Assess the morphology of the erythrocytes.
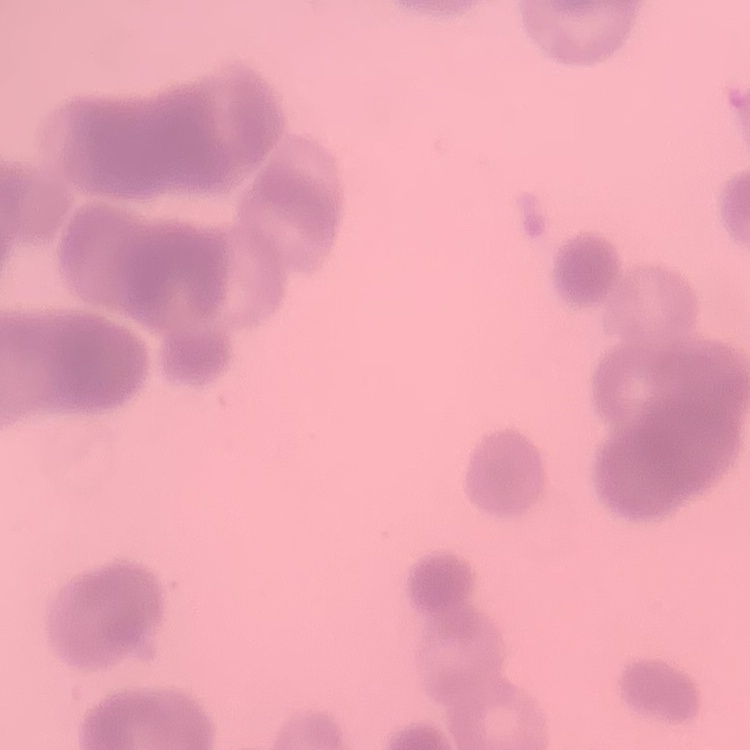
Rouleaux formation.

Summary:
  - Preparation: thin blood film
  - Stain: Field's or Giemsa
  - Image type: square crop of a larger photomicrograph